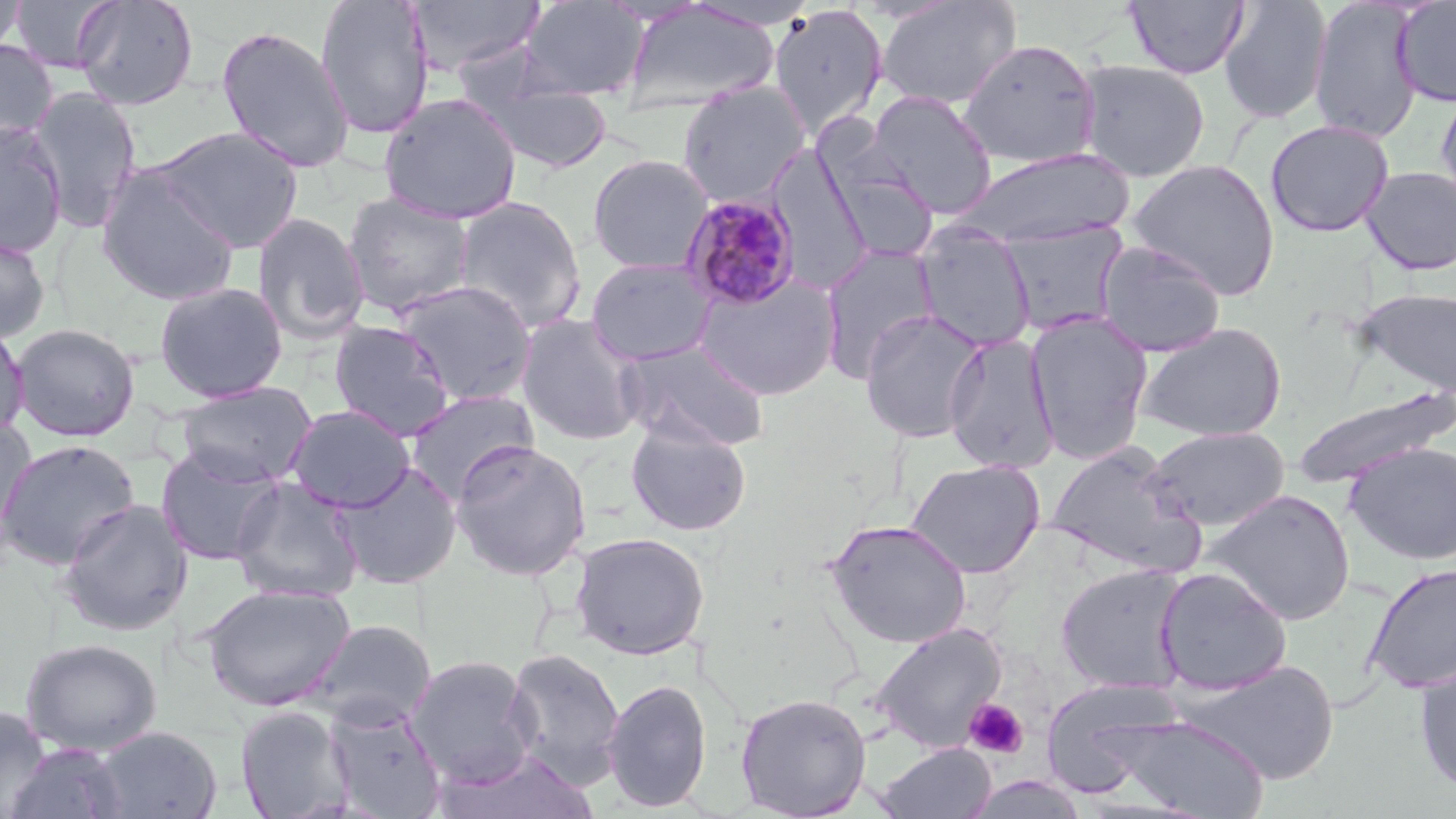
Summary:
  - Coordinate format: approximate bounding boxes as [x1, y1, x2, y2] in pixels
  - Uninfected red blood cell locations: [0, 0, 27, 58], [10, 0, 118, 74], [72, 0, 199, 111], [315, 0, 435, 141], [405, 0, 546, 78], [518, 0, 648, 100], [875, 0, 1021, 110], [1123, 0, 1250, 79], [1218, 0, 1332, 124], [1308, 0, 1423, 144], [1392, 0, 1456, 106], [624, 1, 782, 111], [680, 1, 821, 31], [767, 5, 889, 140], [216, 24, 355, 173], [958, 37, 1102, 169], [0, 39, 58, 148], [1074, 59, 1211, 182], [470, 78, 614, 174], [677, 81, 812, 206], [1434, 82, 1456, 213], [28, 86, 142, 230], [866, 89, 997, 219], [379, 92, 522, 224], [1265, 120, 1394, 237], [0, 122, 68, 259], [150, 125, 304, 254], [948, 147, 1134, 250], [769, 148, 872, 296], [587, 154, 715, 274], [1126, 158, 1281, 300], [1360, 166, 1456, 275], [96, 168, 241, 306], [342, 192, 475, 317], [453, 196, 587, 334], [253, 211, 369, 345], [999, 221, 1130, 338], [913, 223, 1036, 351], [0, 232, 51, 344], [1094, 240, 1228, 358], [819, 243, 940, 382], [586, 257, 718, 366], [695, 273, 842, 401], [392, 279, 538, 405], [153, 281, 289, 402], [1355, 287, 1456, 399], [858, 309, 989, 444], [1024, 311, 1154, 464], [515, 313, 646, 446], [329, 319, 455, 441], [0, 322, 30, 438], [1135, 322, 1287, 442], [10, 323, 141, 442], [942, 331, 1060, 473], [618, 339, 770, 452], [175, 381, 318, 488], [1293, 388, 1451, 491], [404, 390, 539, 502], [285, 404, 416, 512], [0, 416, 36, 536], [625, 418, 751, 537], [1146, 426, 1290, 530], [0, 438, 140, 570], [451, 438, 592, 580], [1045, 441, 1206, 579], [1346, 441, 1456, 565], [156, 445, 286, 567], [906, 458, 1046, 579], [331, 461, 462, 589], [228, 477, 364, 603], [1204, 489, 1357, 624], [57, 498, 192, 636], [824, 518, 972, 649], [569, 531, 710, 660], [1363, 562, 1456, 694], [1055, 564, 1192, 694], [1154, 566, 1293, 695], [200, 583, 355, 711], [306, 619, 436, 730], [871, 621, 1008, 753], [20, 638, 162, 756], [503, 647, 625, 789], [405, 654, 539, 789], [1177, 658, 1340, 785], [1413, 658, 1456, 797], [1040, 677, 1187, 797], [601, 678, 713, 813], [735, 692, 872, 819], [326, 702, 448, 819], [0, 705, 52, 817], [235, 705, 354, 819], [1115, 715, 1268, 819], [93, 726, 222, 819], [6, 741, 130, 819], [876, 742, 997, 819], [436, 748, 596, 819]
  - Plasmodium malariae-infected red blood cell locations: [677, 193, 802, 313]
  - Platelet locations: [963, 698, 1029, 759]
  - Slide-level diagnosis: Plasmodium malariae
  - Image size: 1456×819 pixels
  - Field of view: one of a larger specimen
  - Modality: optical microscopy
  - Preparation: thin blood smear
  - Magnification: 1000x
  - Stain: May-Grünwald-Giemsa